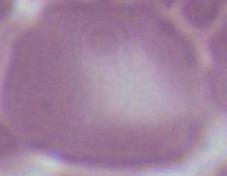

Photomicrograph. Captured at 1000x magnification. An erythrocyte is seen.